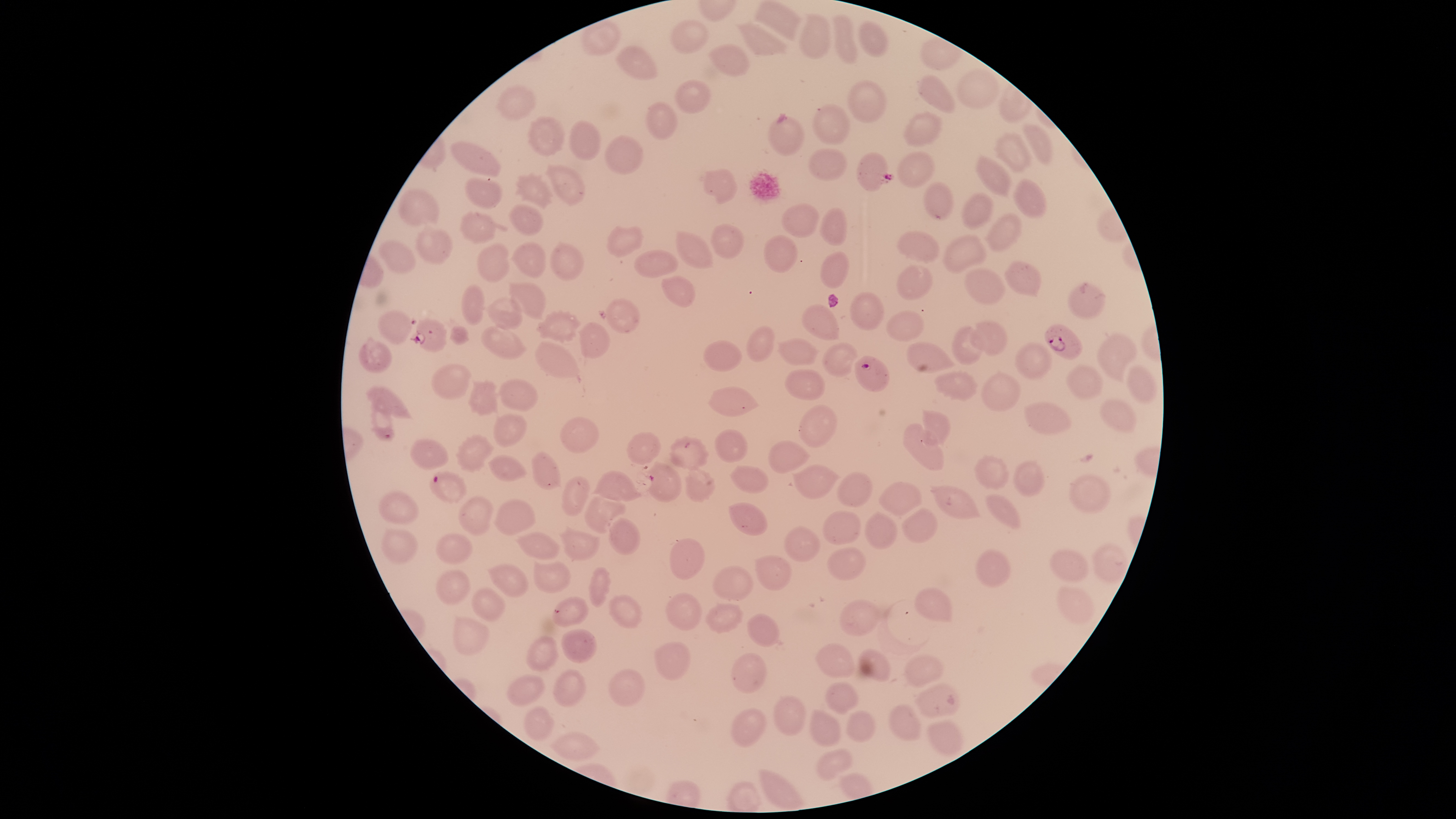
Approximate bounding boxes as {left, top, right, bottom} in pixels. Parasitized RBCs: {857, 152, 893, 192}, {411, 317, 448, 354}, {1045, 323, 1082, 361}, {855, 355, 890, 392}, {430, 472, 468, 504}. Uninfected RBCs: {753, 1, 802, 40}, {799, 12, 831, 59}, {833, 14, 858, 65}, {580, 19, 623, 57}, {671, 20, 709, 53}, {859, 20, 890, 57}, {736, 21, 787, 58}, {707, 44, 750, 76}, {614, 46, 658, 79}, {955, 69, 1000, 109}, {917, 74, 955, 113}, {675, 77, 712, 115}, {846, 80, 888, 123}, {493, 82, 538, 121}, {644, 101, 679, 142}, {811, 103, 851, 144}, {902, 110, 943, 147}, {526, 115, 565, 157}, {768, 116, 805, 155}, {569, 120, 601, 161}, {1022, 122, 1053, 165}, {994, 131, 1033, 174}, {604, 135, 645, 175}, {448, 141, 501, 177}, {807, 148, 849, 182}, {897, 152, 936, 188}, {973, 155, 1011, 196}, {545, 164, 586, 206}, {700, 168, 737, 204}, {514, 171, 554, 209}, {465, 177, 502, 210}, {1013, 177, 1047, 219}, {922, 182, 953, 221}, {397, 188, 440, 228}, {961, 192, 992, 231}, {780, 202, 820, 237}, {508, 204, 544, 236}, {819, 207, 848, 247}, {460, 211, 496, 244}, {985, 213, 1023, 253}, {416, 223, 452, 264}, {710, 223, 744, 258}, {606, 225, 643, 258}, {675, 230, 714, 269}, {897, 231, 939, 262}, {763, 235, 798, 272}, {941, 235, 986, 274}, {550, 240, 585, 281}, {377, 241, 417, 276}, {510, 241, 547, 279}, {476, 243, 509, 283}, {634, 248, 679, 279}, {820, 252, 850, 289}, {1003, 262, 1042, 297}, {896, 264, 932, 301}, {963, 267, 1006, 305}, {661, 275, 697, 308}, {1066, 279, 1107, 317}, {507, 282, 546, 319}, {461, 284, 484, 326}, {849, 292, 884, 331}, {485, 296, 523, 331}, {606, 297, 640, 334}, {802, 304, 839, 342}, {534, 309, 582, 345}, {377, 310, 412, 345}, {887, 310, 923, 343}, {967, 319, 1007, 356}, {577, 321, 610, 359}, {480, 324, 527, 360}, {450, 325, 470, 346}, {746, 325, 776, 362}, {951, 325, 981, 364}, {1097, 334, 1138, 384}, {777, 337, 819, 366}, {359, 338, 393, 373}, {702, 339, 744, 372}, {535, 341, 580, 379}, {905, 341, 959, 373}, {1012, 341, 1053, 381}, {822, 342, 858, 377}, {430, 362, 472, 400}, {1065, 364, 1102, 398}, {1126, 365, 1159, 404}, {784, 368, 826, 402}, {934, 370, 979, 403}, {980, 372, 1021, 412}, {499, 378, 538, 411}, {466, 379, 498, 417}, {705, 384, 761, 418}, {367, 386, 414, 420}, {369, 389, 395, 443}, {1099, 399, 1138, 434}, {1023, 401, 1073, 436}, {799, 405, 837, 446}, {921, 408, 951, 449}, {493, 414, 526, 446}, {560, 417, 600, 453}, {902, 423, 944, 469}, {713, 429, 748, 463}, {626, 432, 662, 466}, {454, 433, 495, 472}, {669, 436, 709, 468}, {410, 439, 449, 471}, {767, 439, 811, 474}, {531, 452, 561, 490}, {487, 454, 527, 481}, {974, 455, 1009, 491}, {1013, 459, 1045, 497}, {644, 461, 683, 503}, {729, 465, 768, 493}, {789, 465, 841, 500}, {684, 468, 717, 504}, {591, 470, 644, 502}, {837, 472, 872, 508}, {561, 474, 588, 517}, {1069, 474, 1111, 513}, {878, 482, 922, 516}, {930, 485, 982, 520}, {377, 491, 419, 525}, {985, 492, 1021, 531}, {457, 495, 494, 535}, {585, 495, 626, 534}, {494, 499, 536, 536}, {729, 501, 767, 535}, {821, 508, 862, 547}, {901, 508, 938, 543}, {863, 511, 899, 549}, {608, 516, 640, 555}, {560, 526, 600, 561}, {782, 526, 821, 563}, {378, 527, 421, 563}, {515, 531, 559, 560}, {436, 533, 472, 564}, {669, 537, 706, 580}, {1091, 542, 1130, 586}, {1049, 546, 1090, 583}, {826, 547, 866, 581}, {975, 550, 1012, 589}, {755, 556, 792, 590}, {533, 560, 570, 593}, {487, 563, 532, 598}, {712, 565, 755, 602}, {589, 567, 612, 608}, {435, 570, 470, 604}, {1056, 586, 1095, 625}, {914, 587, 953, 624}, {471, 588, 506, 621}, {665, 592, 702, 631}, {606, 593, 641, 630}, {551, 597, 589, 626}, {838, 599, 880, 637}, {704, 603, 743, 634}, {745, 613, 780, 648}, {453, 614, 490, 655}, {561, 628, 600, 665}, {524, 636, 559, 672}, {653, 641, 690, 681}, {815, 642, 856, 679}, {858, 647, 891, 681}, {731, 653, 767, 694}, {903, 654, 945, 687}, {552, 668, 587, 706}, {608, 668, 645, 707}, {506, 673, 546, 707}, {824, 682, 858, 716}, {915, 683, 960, 718}, {771, 694, 806, 736}, {888, 703, 921, 742}, {524, 706, 555, 741}, {731, 708, 767, 748}, {845, 708, 877, 743}, {810, 709, 842, 748}, {927, 720, 964, 757}, {551, 731, 600, 760}, {816, 748, 854, 781}, {760, 768, 805, 811}. Presence: malaria parasites detected. Circular visible region. Thin blood smear. Smartphone photograph through the microscope eyepiece. Species: Plasmodium falciparum. Image is 1456×819 pixels. One field of view of the specimen. Giemsa-stained preparation.